Name the cell type shown.
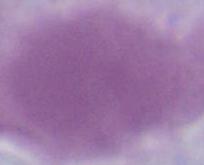

An erythrocyte.

modality = photomicrograph
magnification = 1000x